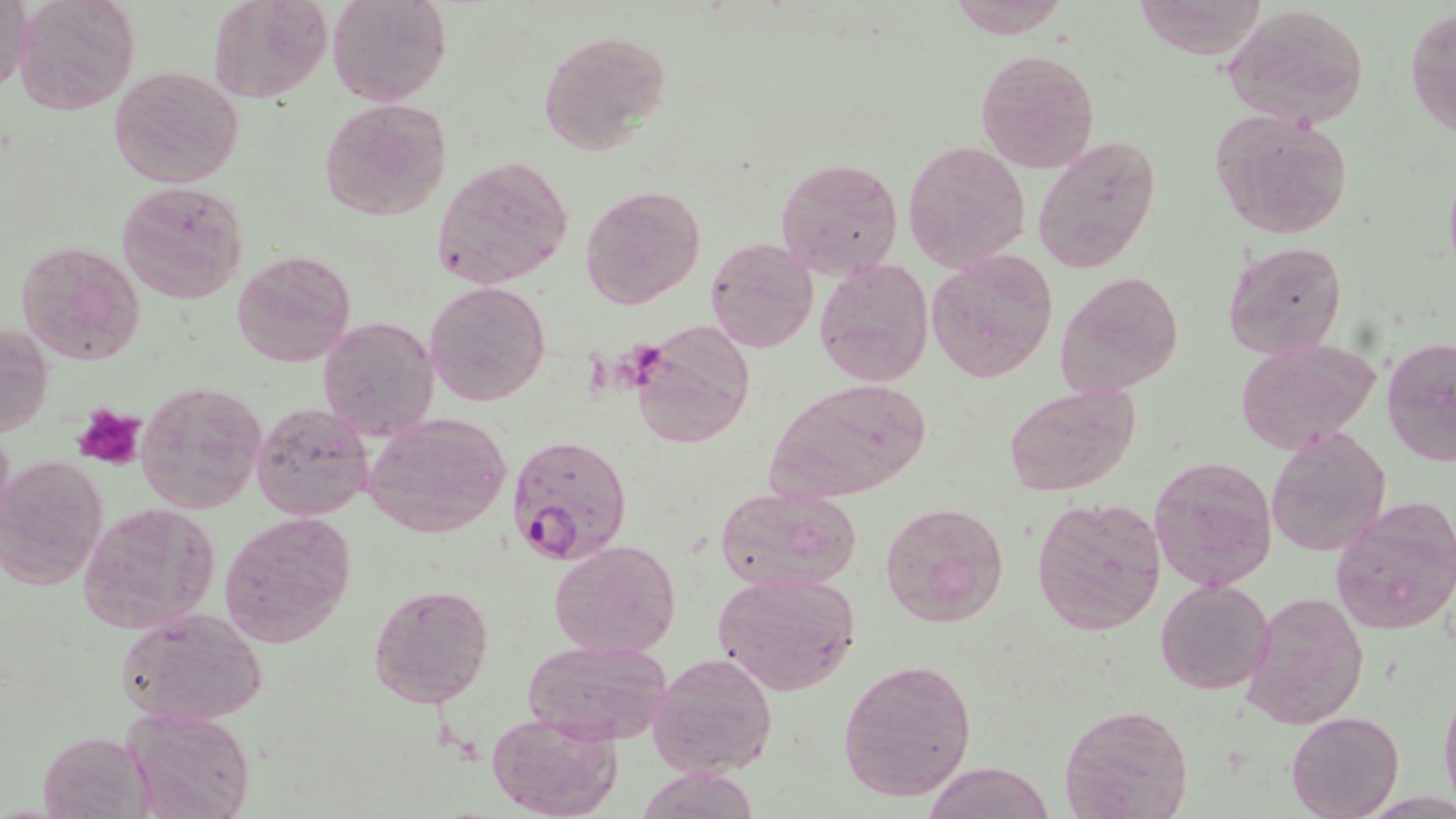

Plasmodium falciparum-infected red blood cell locations = approximate bounding boxes as [x1, y1, x2, y2] in pixels: [505, 432, 632, 563]
slide-level diagnosis = Plasmodium falciparum
field of view = one of a larger specimen
preparation = thin blood smear
uninfected red blood cell locations = approximate bounding boxes as [x1, y1, x2, y2] in pixels: [13, 0, 139, 116], [209, 0, 331, 104], [326, 0, 451, 107], [1, 1, 37, 96], [943, 2, 1072, 36], [1222, 4, 1371, 127], [1406, 6, 1455, 141], [538, 27, 671, 157], [977, 48, 1099, 174], [108, 65, 244, 188], [319, 98, 453, 221], [1210, 109, 1357, 240], [1032, 134, 1164, 272], [903, 141, 1030, 272], [432, 156, 574, 288], [776, 157, 905, 281], [1441, 166, 1456, 274], [117, 182, 249, 304], [579, 182, 707, 310], [704, 236, 818, 354], [15, 240, 145, 366], [1223, 241, 1348, 358], [232, 251, 357, 370], [928, 251, 1058, 382], [814, 257, 934, 387], [1055, 270, 1185, 399], [427, 280, 548, 405], [317, 315, 439, 443], [629, 322, 757, 448], [0, 323, 51, 436], [1383, 335, 1456, 467], [1233, 338, 1380, 457], [136, 379, 267, 513], [768, 379, 931, 500], [1005, 383, 1141, 499], [252, 403, 373, 521], [360, 411, 513, 541], [1266, 426, 1391, 558], [0, 455, 106, 589], [1148, 455, 1278, 593], [715, 485, 861, 594], [1031, 496, 1168, 635], [1330, 499, 1456, 633], [78, 500, 223, 634], [878, 501, 1010, 626], [219, 512, 358, 647], [548, 539, 680, 659], [711, 571, 862, 697], [1156, 578, 1273, 695], [367, 581, 494, 709], [1239, 589, 1369, 731], [114, 607, 268, 729], [521, 638, 674, 746], [647, 652, 777, 776], [837, 658, 977, 803], [1439, 682, 1456, 815], [1059, 702, 1194, 819], [124, 707, 255, 818], [487, 711, 623, 819], [1286, 711, 1403, 819], [38, 730, 151, 817], [922, 760, 1058, 819], [634, 767, 765, 819]
image size = 1456×819 pixels
modality = optical microscopy
stain = May-Grünwald-Giemsa
platelet locations = approximate bounding boxes as [x1, y1, x2, y2] in pixels: [73, 403, 147, 471]
magnification = 1000x